Outline each uninfected red blood cell.
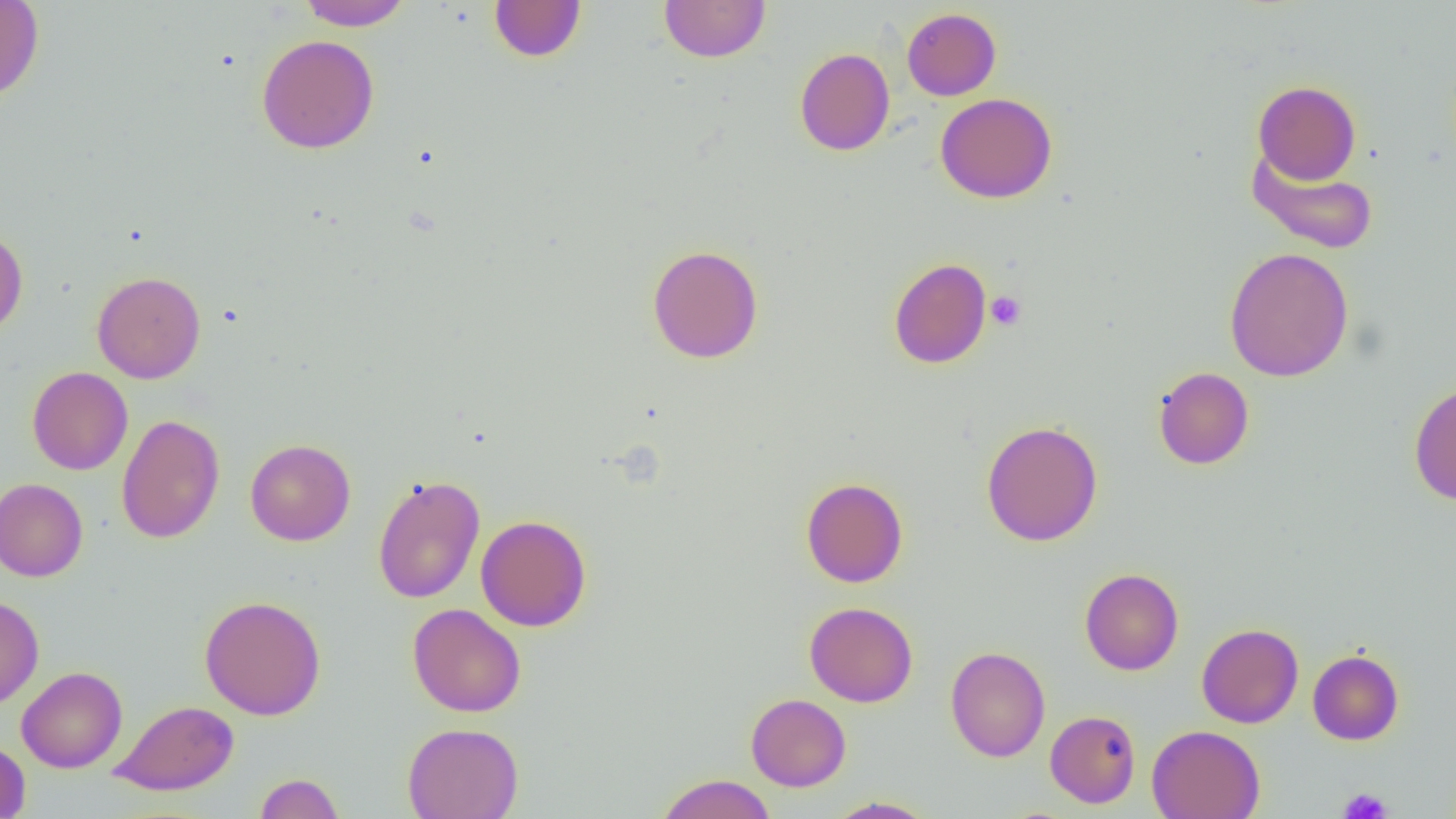

Approximate bounding boxes as named x1/y1/x2/y2 corners in pixels.
Uninfected red blood cells: (x1=0, y1=0, x2=44, y2=103), (x1=298, y1=0, x2=412, y2=30), (x1=658, y1=0, x2=771, y2=63), (x1=489, y1=1, x2=586, y2=62), (x1=902, y1=8, x2=1001, y2=101), (x1=256, y1=34, x2=379, y2=154), (x1=794, y1=47, x2=895, y2=156), (x1=1253, y1=80, x2=1361, y2=184), (x1=934, y1=93, x2=1058, y2=203), (x1=1246, y1=147, x2=1379, y2=256), (x1=0, y1=226, x2=28, y2=337), (x1=646, y1=244, x2=763, y2=363), (x1=1224, y1=247, x2=1354, y2=382), (x1=888, y1=257, x2=992, y2=369), (x1=92, y1=270, x2=206, y2=383), (x1=27, y1=366, x2=132, y2=475), (x1=1153, y1=366, x2=1254, y2=470), (x1=1408, y1=380, x2=1456, y2=505), (x1=116, y1=414, x2=225, y2=544), (x1=980, y1=420, x2=1104, y2=546), (x1=245, y1=439, x2=356, y2=545), (x1=372, y1=474, x2=485, y2=604), (x1=801, y1=477, x2=908, y2=588), (x1=0, y1=478, x2=88, y2=581), (x1=475, y1=515, x2=591, y2=631), (x1=1080, y1=568, x2=1183, y2=675), (x1=0, y1=595, x2=44, y2=709), (x1=199, y1=595, x2=326, y2=720), (x1=803, y1=601, x2=918, y2=707), (x1=408, y1=603, x2=526, y2=717), (x1=1197, y1=623, x2=1303, y2=728), (x1=945, y1=646, x2=1050, y2=762), (x1=1307, y1=649, x2=1404, y2=745), (x1=17, y1=666, x2=127, y2=773), (x1=746, y1=693, x2=851, y2=791), (x1=110, y1=700, x2=239, y2=796), (x1=1045, y1=710, x2=1141, y2=808), (x1=402, y1=722, x2=524, y2=819), (x1=1147, y1=725, x2=1265, y2=818), (x1=0, y1=739, x2=31, y2=819), (x1=255, y1=773, x2=345, y2=818), (x1=655, y1=773, x2=777, y2=819), (x1=824, y1=796, x2=938, y2=818).

Platelet locations: (x1=985, y1=291, x2=1026, y2=330), (x1=1338, y1=787, x2=1392, y2=819). Slide-level diagnosis: no evidence of blood parasites. One field of a larger specimen. Thin blood smear. Image is 1456×819 pixels. Light microscopy. Captured at 1000x magnification.